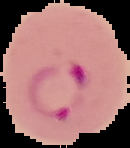 Result: Plasmodium parasites detected. Segmented cell region on a black background. From a thin blood film. Image is 130×148 pixels.